Name the cell type shown.
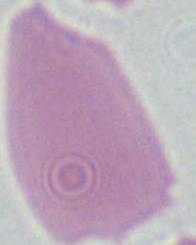
This is an erythrocyte.

magnification = 1000x
modality = photomicrograph